Find the cells and give the type of each one.
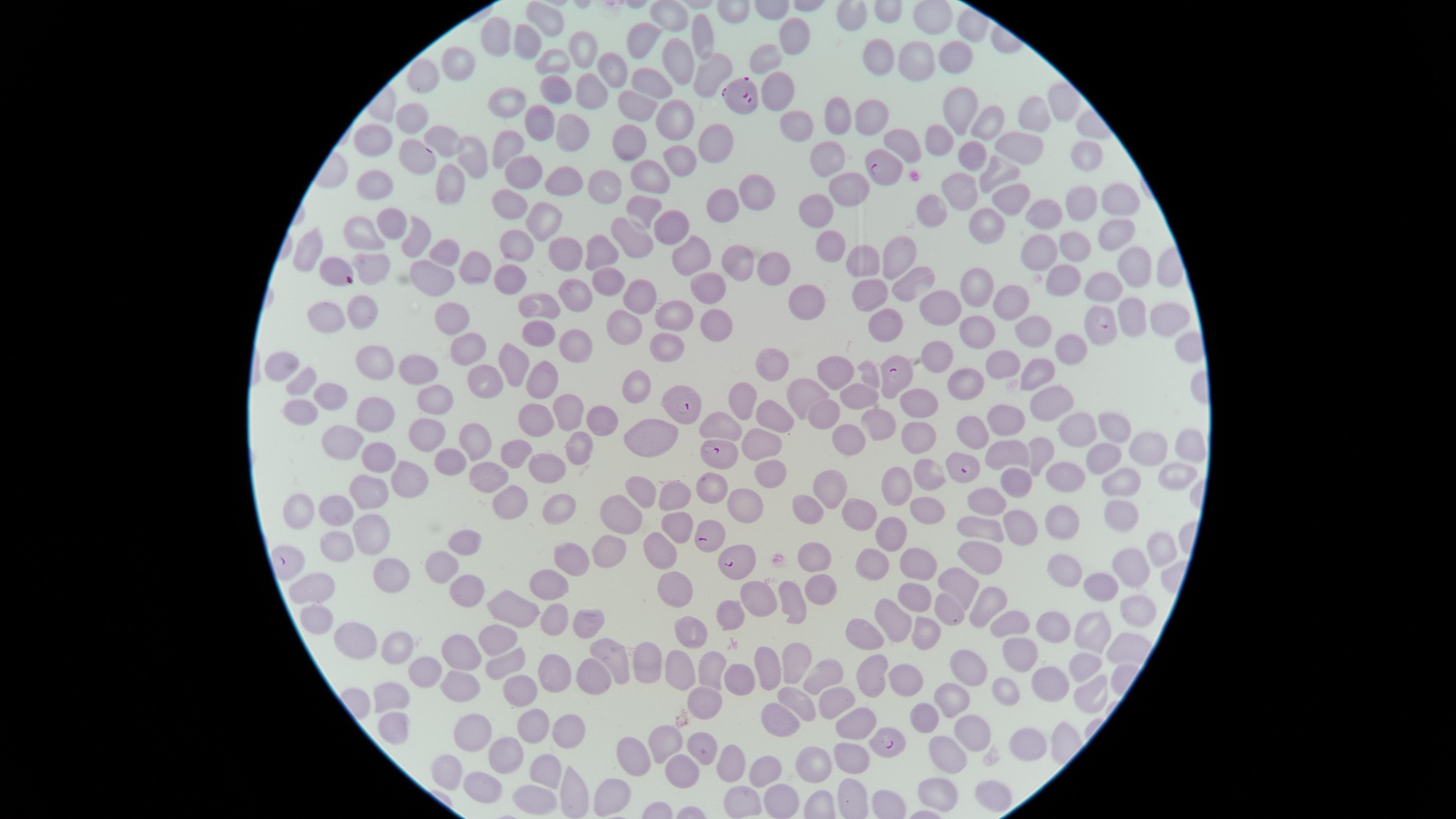

Approximate marker points as [x, y] in pixels.
Parasitized red blood cells: [744, 93], [412, 156], [884, 170], [1097, 329], [893, 375], [681, 405], [719, 454], [962, 469], [706, 533], [736, 563], [885, 744].
Uninfected red blood cells: [668, 15], [549, 19], [499, 35], [790, 36], [702, 41], [646, 42], [528, 44], [584, 46], [944, 54], [881, 55], [771, 57], [554, 62], [673, 64], [915, 69], [710, 70], [459, 71], [610, 72], [424, 77], [654, 79], [554, 85], [785, 87], [591, 91], [507, 103], [640, 105], [960, 112], [1024, 114], [672, 115], [874, 118], [989, 118], [412, 119], [836, 121], [539, 124], [571, 127], [806, 129], [441, 137], [943, 137], [897, 144], [632, 145], [373, 146], [507, 146], [725, 150], [677, 152], [1020, 153], [1080, 154], [826, 157], [466, 158], [972, 160], [999, 171], [522, 173], [557, 176], [652, 178], [448, 185], [854, 188], [962, 188], [759, 189], [379, 190], [608, 190], [1008, 196], [518, 202], [1108, 204], [726, 206], [821, 207], [1078, 207], [938, 209], [648, 211], [1041, 212], [545, 218], [391, 222], [982, 222], [672, 225], [1114, 234], [366, 237], [416, 239], [634, 244], [523, 245], [832, 246], [899, 248], [568, 250], [1041, 251], [1076, 251], [310, 252], [443, 252], [604, 254], [695, 254], [862, 258], [475, 262], [1131, 264], [740, 267], [378, 269], [774, 269], [435, 276], [510, 278], [1054, 279], [608, 283], [907, 284], [710, 287], [1097, 288], [639, 292], [871, 293], [983, 293], [573, 295], [539, 303], [812, 304], [944, 307], [1012, 310], [365, 312], [1128, 313], [678, 314], [326, 315], [716, 316], [1162, 317], [452, 319], [882, 319], [982, 327], [538, 330], [628, 331], [1037, 333], [578, 342], [676, 346], [1074, 347], [466, 350], [941, 358], [1001, 363], [381, 364], [521, 364], [289, 365], [771, 365], [1030, 371], [420, 372], [832, 376], [303, 380], [490, 380], [963, 380], [543, 385], [335, 390], [640, 390], [812, 393], [859, 396], [743, 400], [1047, 400], [436, 401], [913, 406], [301, 411], [373, 413], [821, 414], [535, 416], [776, 416], [570, 417], [1008, 418], [602, 421], [876, 425], [1109, 425], [1075, 426], [654, 427], [720, 427], [974, 427], [765, 437], [847, 439], [915, 439], [342, 440], [429, 440], [1140, 440], [477, 442], [1184, 442], [582, 449], [1041, 449], [1009, 452], [519, 454], [1097, 454], [382, 455], [453, 457], [1173, 466], [549, 469], [768, 474], [487, 475], [927, 477], [1076, 479], [410, 480], [1124, 480], [1014, 485], [709, 489], [903, 489], [828, 490], [639, 493], [371, 497], [676, 503], [512, 505], [988, 505], [560, 508], [746, 508], [1121, 508], [333, 509], [808, 510], [299, 513], [927, 513], [621, 517], [1062, 517], [861, 521], [1021, 521], [674, 527], [988, 529], [365, 531], [893, 534], [467, 541], [333, 548], [614, 548], [1153, 548], [659, 549], [815, 553], [984, 553], [872, 556], [568, 560], [918, 561], [1128, 566], [442, 568], [393, 571], [1072, 571], [1100, 583], [548, 585], [817, 585], [963, 585], [674, 589], [317, 591], [913, 593], [472, 596], [756, 600], [792, 602], [984, 602], [514, 607], [942, 607], [1132, 607], [730, 616], [549, 617], [1008, 618], [581, 621], [897, 622], [317, 623], [1091, 623], [1061, 627], [690, 628], [925, 632], [871, 635], [357, 639], [489, 641], [615, 652], [460, 654], [400, 655], [1015, 656], [1079, 659], [647, 660], [795, 662], [503, 664], [709, 664], [974, 665], [769, 668], [430, 670], [555, 671], [678, 673], [820, 673], [588, 677], [905, 677], [1053, 677], [873, 680], [738, 682], [460, 687], [1004, 689], [1092, 691], [965, 696], [522, 697], [392, 701], [845, 703], [704, 704], [795, 704], [781, 721], [930, 721], [857, 724], [533, 726], [566, 727], [393, 734], [972, 737], [475, 740], [1030, 740], [677, 741], [702, 745], [850, 756], [636, 757], [733, 762], [949, 762], [511, 763], [545, 766], [823, 767], [450, 768], [763, 771], [682, 774], [489, 783], [998, 788], [575, 792], [935, 795], [615, 797], [743, 797], [786, 798], [540, 803].
No white blood cells identified.

Giemsa-stained preparation. Image is 1456×819 pixels. One field of view of the specimen. Smartphone photograph through the microscope eyepiece. Species: Plasmodium falciparum. The visible region is circular. Thin smear of blood.